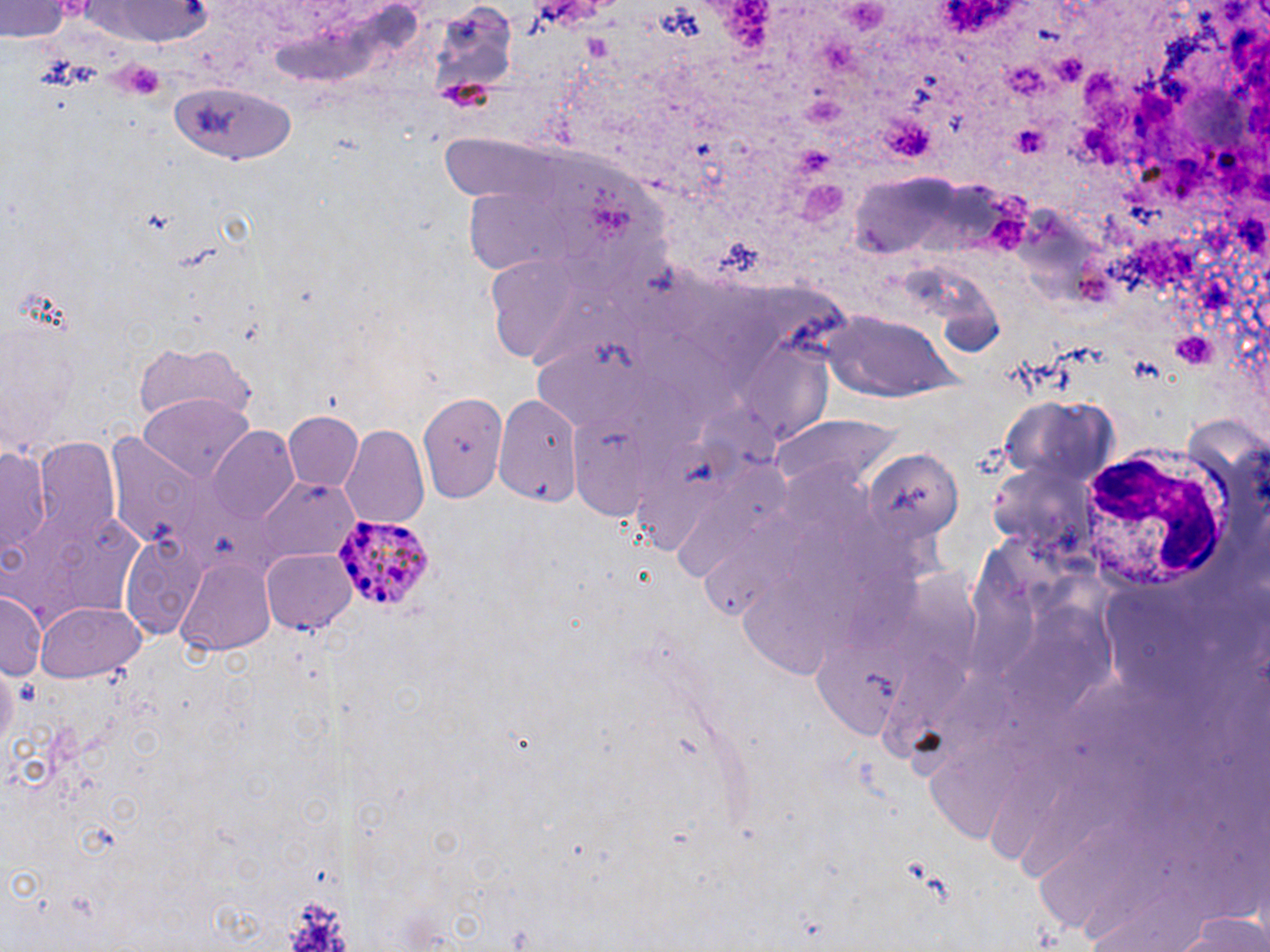

{
  "slide_level_diagnosis": "Plasmodium ovale",
  "stain": "May-Grünwald-Giemsa",
  "uninfected_red_blood_cell_locations": "approximate bounding boxes as (x1,y1)-(x2,y2) corner pairs in pixels: (3,0)-(71,43), (82,3)-(220,45), (166,79)-(300,162), (445,141)-(678,299), (821,313)-(963,403), (1,323)-(84,456), (133,341)-(252,429), (494,391)-(582,503), (418,392)-(506,505), (139,395)-(254,484), (284,410)-(365,491), (771,417)-(899,497), (340,423)-(430,530), (207,425)-(300,522), (33,438)-(121,545), (1,444)-(51,559), (864,446)-(964,547), (259,478)-(360,564), (8,510)-(146,623), (117,530)-(212,640), (262,547)-(358,634), (176,556)-(277,655), (1,589)-(46,681), (35,600)-(145,683)",
  "plasmodium_ovale_infected_red_blood_cell_locations": "approximate bounding boxes as (x1,y1)-(x2,y2) corner pairs in pixels: (332,514)-(436,611)",
  "platelet_locations": "approximate bounding boxes as (x1,y1)-(x2,y2) corner pairs in pixels: (841,0)-(891,32), (817,38)-(855,70), (1054,53)-(1085,86), (115,58)-(167,99), (1002,62)-(1048,101), (801,96)-(844,124), (882,115)-(935,158), (1012,125)-(1051,158), (790,141)-(832,174), (798,181)-(847,226), (1171,331)-(1222,371), (279,887)-(356,952)",
  "modality": "light microscopy",
  "image_size": "1270×952 pixels",
  "field_of_view": "one of a larger specimen",
  "white_blood_cell_locations": "approximate bounding boxes as (x1,y1)-(x2,y2) corner pairs in pixels: (1076,441)-(1229,592)",
  "magnification": "1000x",
  "preparation": "thin blood film"
}